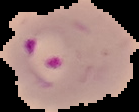 Image is 139×112 pixels. Segmented cell region on a black background. From a thin blood smear. Malaria status: parasitized.